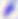

Captured at 400x magnification. Toxoplasma gondii is shown. Photomicrograph.